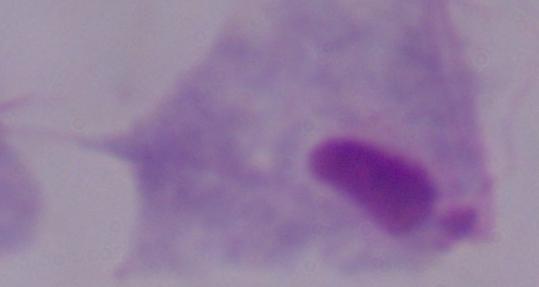

Summary:
  - Magnification: 1000x
  - Identification: trichomonad
  - Modality: micrograph